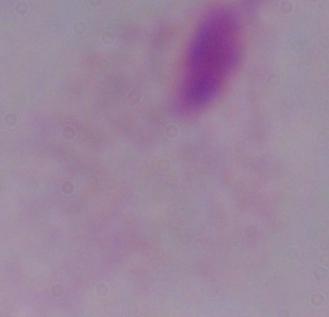

Photomicrograph. Captured at 1000x magnification. A trichomonad is seen.